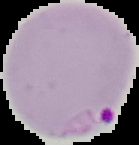
preparation = thin blood film
image type = segmented cell region on a black background
malaria status = parasitized
image size = 139×145 pixels